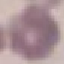

result: no malaria parasites detected
image_type: automatically extracted cell patch, resized to 64 × 64 pixels
capture: smartphone camera at the microscope eyepiece
stain: Giemsa
preparation: thin blood film